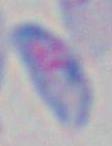

modality = micrograph
identification = Toxoplasma gondii
magnification = 1000x